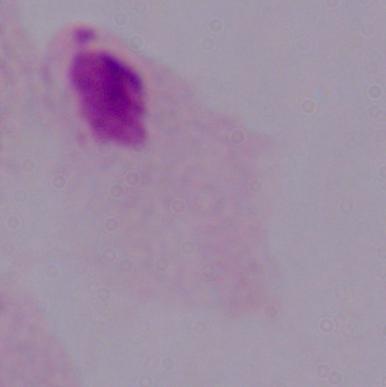
Summary:
  - Identification: trichomonad
  - Modality: micrograph
  - Magnification: 1000x